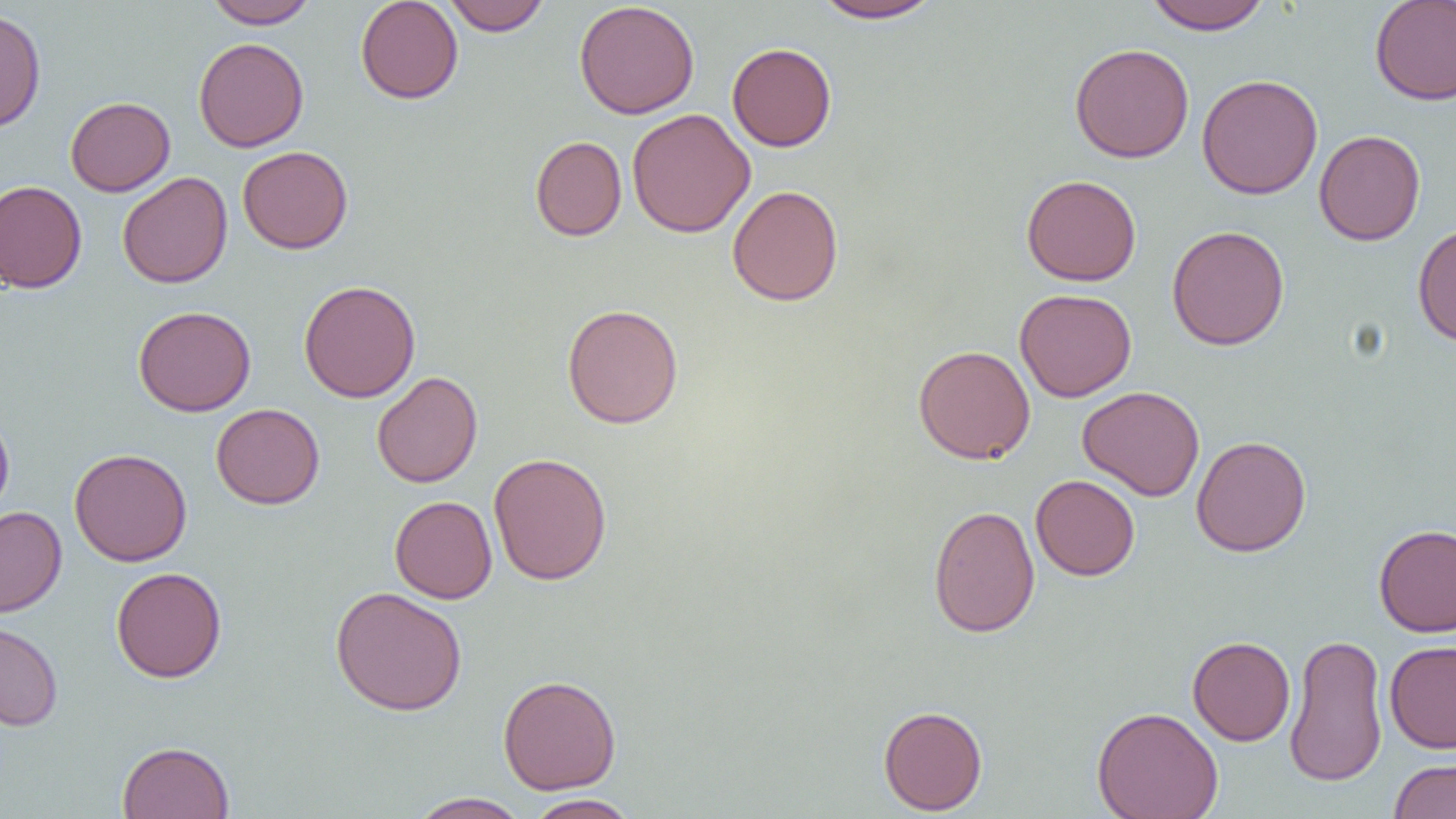

slide-level diagnosis = negative for blood parasites
image size = 1456×819 pixels
uninfected red blood cell locations = approximate bounding boxes as (x1, y1, x2, y2) in pixels: (203, 0, 319, 28), (355, 0, 463, 104), (443, 0, 550, 35), (811, 0, 946, 24), (1143, 0, 1272, 33), (1369, 0, 1456, 106), (574, 1, 700, 119), (0, 7, 46, 133), (193, 37, 309, 152), (727, 42, 837, 152), (1069, 43, 1194, 163), (1196, 74, 1323, 199), (65, 96, 175, 196), (628, 108, 756, 238), (1314, 129, 1425, 246), (530, 136, 627, 241), (237, 146, 353, 254), (117, 172, 233, 288), (1021, 174, 1141, 286), (0, 180, 87, 293), (727, 185, 844, 306), (1412, 222, 1456, 346), (1167, 224, 1290, 350), (298, 280, 421, 403), (1015, 288, 1137, 402), (562, 303, 684, 429), (133, 305, 257, 416), (913, 344, 1035, 464), (371, 371, 483, 488), (1078, 385, 1205, 501), (211, 403, 325, 509), (0, 410, 15, 522), (1191, 435, 1312, 557), (68, 448, 192, 566), (488, 452, 612, 585), (1031, 474, 1140, 581), (390, 495, 497, 604), (928, 504, 1040, 638), (0, 506, 67, 617), (1373, 523, 1456, 637), (111, 566, 226, 683), (330, 586, 467, 716), (0, 622, 63, 731), (1284, 632, 1388, 788), (1187, 636, 1295, 746), (1384, 641, 1456, 754), (497, 674, 622, 794), (878, 705, 987, 815), (1092, 706, 1223, 819), (116, 741, 234, 819), (1388, 759, 1456, 819), (409, 792, 531, 819), (524, 794, 640, 819)
magnification = 1000x
field of view = one of a larger specimen
modality = optical microscopy
preparation = thin blood smear